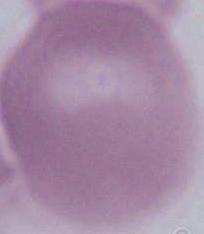

modality = photomicrograph
identification = red blood cell
magnification = 1000x